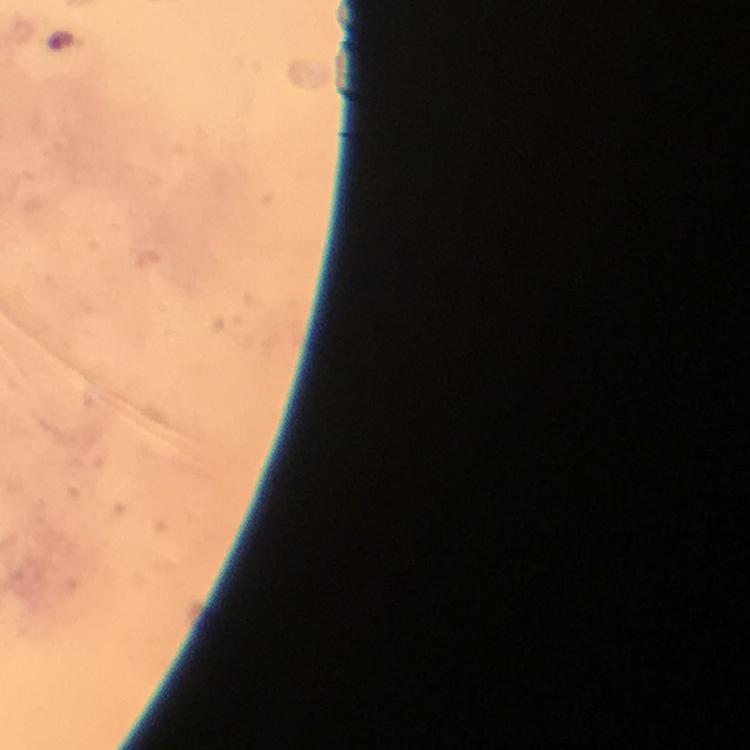

magnification: 100x
malaria_parasite_locations: 'approximate object centers, in pixels from the top-left corner: (x=60, y=41)'
context: from a diagnostic examination for malaria
capture: smartphone photograph through a microscope
preparation: thick blood smear
image_size: 750×750 pixels
cropped_from: a single field of view
stain: Giemsa
immersion_oil: used